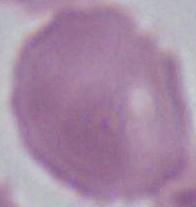
Summary:
  - Modality: micrograph
  - Magnification: 1000x
  - Identification: erythrocyte